Identify the blood parasite species.
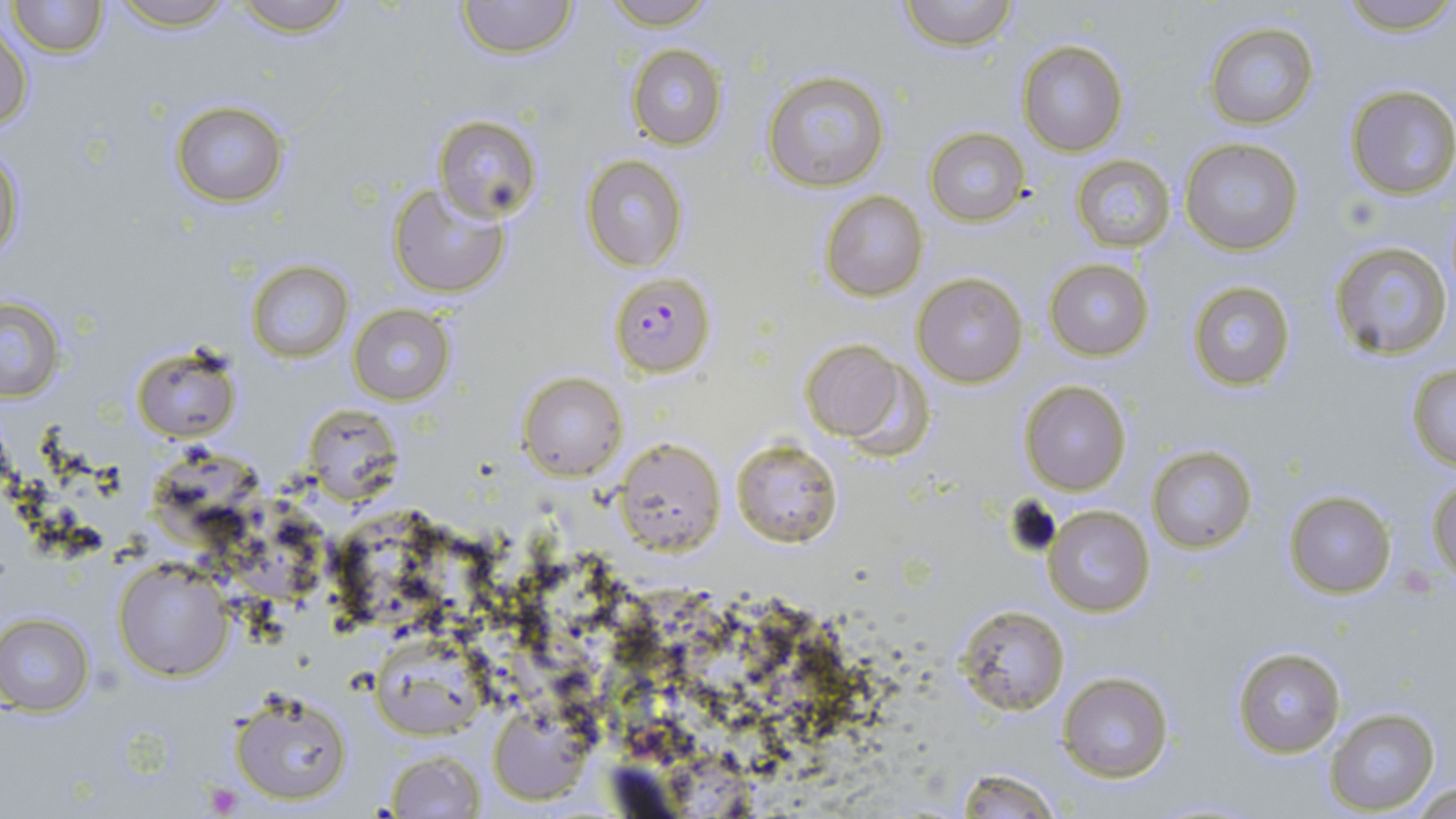
Plasmodium falciparum.

Approximate bounding boxes as (x1, y1, x2, y2) in pixels. Platelet locations: (1398, 564, 1441, 598), (203, 779, 243, 814). Uninfected red blood cell locations: (8, 0, 107, 57), (107, 0, 240, 31), (227, 0, 359, 36), (599, 0, 722, 29), (898, 0, 1018, 51), (1340, 0, 1456, 36), (455, 1, 577, 59), (1, 22, 34, 134), (1202, 22, 1320, 130), (1018, 39, 1128, 155), (626, 45, 727, 149), (761, 69, 889, 191), (1344, 85, 1456, 200), (170, 101, 290, 205), (432, 114, 540, 222), (924, 128, 1031, 227), (1179, 136, 1304, 255), (0, 142, 25, 267), (1071, 154, 1176, 253), (581, 155, 687, 271), (387, 181, 512, 297), (818, 191, 929, 302), (1327, 240, 1453, 360), (1044, 258, 1153, 359), (246, 259, 353, 364), (913, 273, 1027, 387), (1186, 282, 1296, 390), (1, 297, 64, 402), (348, 304, 455, 405), (799, 340, 917, 448), (130, 343, 241, 443), (1405, 363, 1456, 470), (518, 371, 628, 480), (1020, 382, 1132, 495), (616, 436, 726, 556), (732, 439, 843, 549), (1147, 445, 1257, 552), (1428, 479, 1456, 582), (1283, 489, 1397, 598), (1042, 503, 1155, 618), (114, 558, 231, 681), (955, 604, 1069, 715), (0, 613, 96, 714), (370, 640, 485, 742), (1232, 647, 1345, 757), (1058, 672, 1173, 782), (227, 688, 354, 806), (488, 704, 593, 804), (1323, 707, 1440, 814), (383, 750, 488, 816), (951, 766, 1064, 818), (1406, 780, 1454, 817). Plasmodium falciparum-infected red blood cell locations: (607, 271, 716, 376). Thin blood smear. Image is 1456×819 pixels. May-Grünwald-Giemsa stain. Optical microscopy. Single field of view. Captured at 1000x magnification.